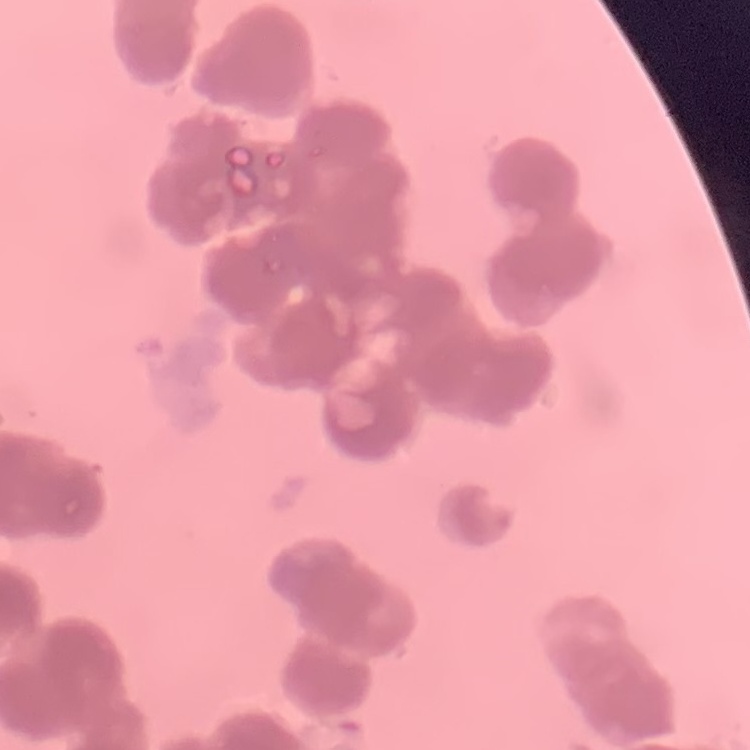

Summary:
  - Erythrocyte morphology: rouleaux formation
  - Preparation: thin peripheral smear
  - Stain: Field's or Giemsa
  - Image type: one tile cut from a larger photomicrograph